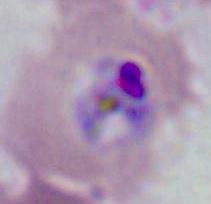

{
  "modality": "photomicrograph",
  "magnification": "400x or 1000x",
  "identification": "Plasmodium"
}